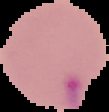

Summary:
  - Image size: 109×112 pixels
  - Result: malaria parasites identified
  - Preparation: thin blood film
  - Image type: segmented cell region with the area outside set to black